Assess the morphology of the red blood cells.
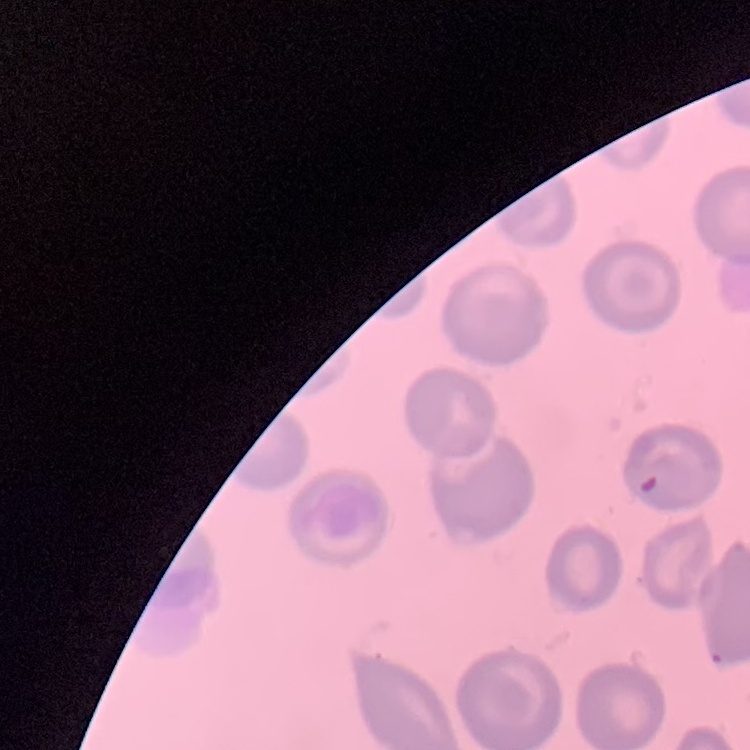
They show no rouleaux formation.

preparation = thin blood film
image type = square crop of a larger photomicrograph
stain = Field's or Giemsa